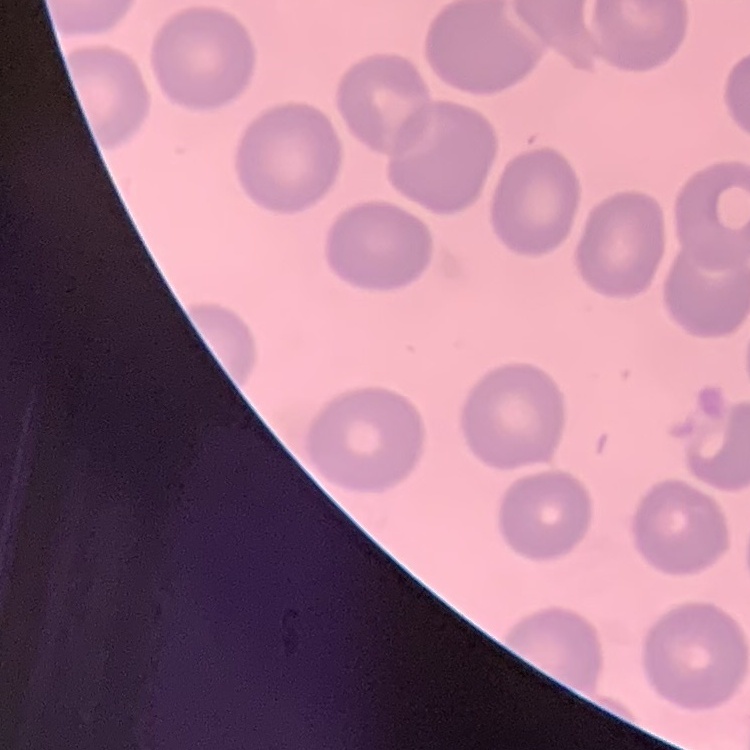
Summary:
  - Erythrocyte morphology: no rouleaux formation
  - Preparation: thin blood smear
  - Image type: one tile cut from a larger photomicrograph
  - Stain: Field's or Giemsa